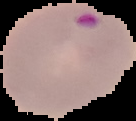

image_type: segmented cell region with the area outside set to black
preparation: thin blood film
image_size: 136×121 pixels
result: Plasmodium parasites detected